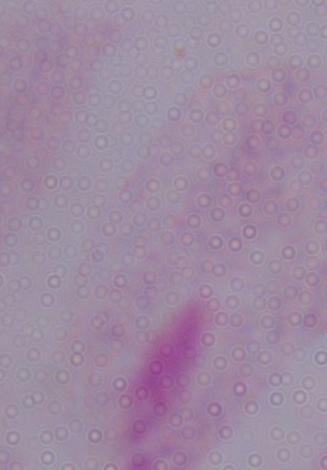
Summary:
  - Modality: photomicrograph
  - Magnification: 1000x
  - Identification: trichomonad